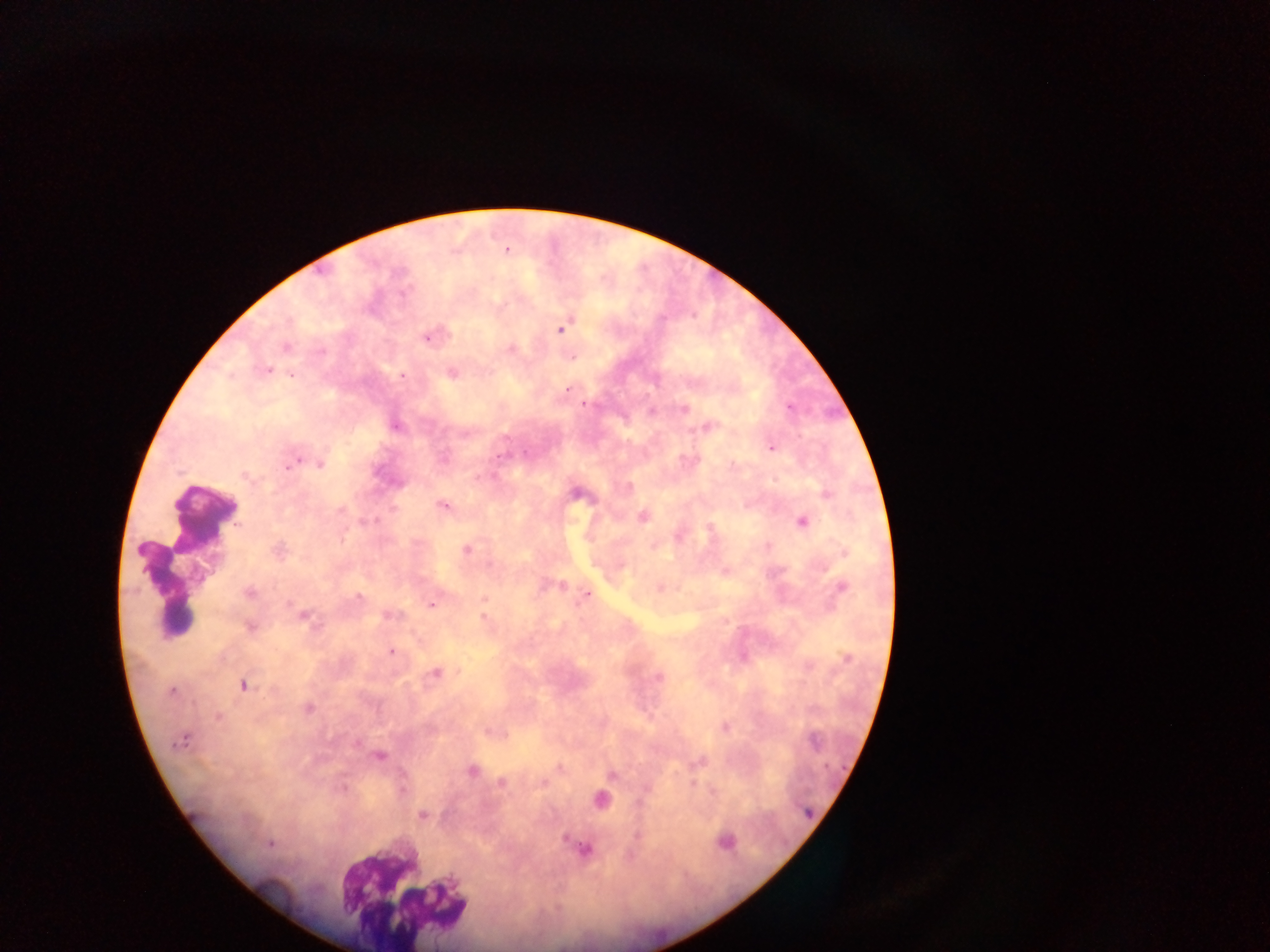
{
  "country": "Ghana",
  "capture": "mobile-phone photograph through a microscope",
  "image_size": "1270×952 pixels",
  "leukocyte_locations": "approximate centers as x y in pixels (subset; some below the resolvable size): 204 513; 164 586",
  "field_of_view": "single",
  "preparation": "thick blood smear",
  "plasmodium_parasite_locations": "approximate centers as x y in pixels: 506 250; 403 293; 561 329; 427 337; 286 347; 510 349; 266 369; 452 373; 291 374; 402 375; 567 389; 585 404; 789 407; 684 409; 395 426; 771 448; 293 463; 320 464; 245 477; 575 493; 444 505; 341 509; 231 510; 643 516; 802 521; 467 549; 278 551; 562 585; 662 587; 841 588; 249 592; 587 595; 359 596; 484 600; 431 605; 305 617; 484 618; 249 627; 391 651; 846 658; 457 672; 435 673; 659 677; 243 686; 172 691; 308 708; 217 716; 726 727; 488 731; 181 741; 380 756; 472 771; 613 776; 501 783; 343 790; 601 799; 808 812; 423 815; 725 842; 270 844"
}